Identify the cell.
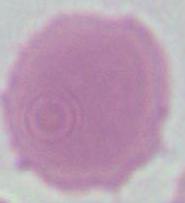

This is an erythrocyte.

Summary:
  - Modality: photomicrograph
  - Magnification: 1000x